Assess the morphology of the erythrocytes.
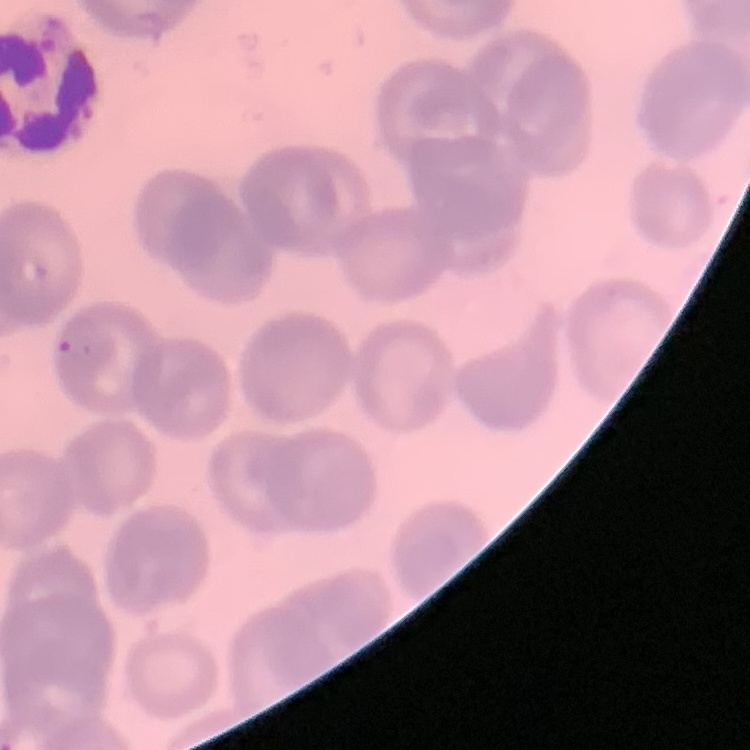

They show no rouleaux formation.

{
  "image_type": "one tile cut from a larger photomicrograph",
  "preparation": "thin peripheral smear",
  "stain": "Field's or Giemsa"
}